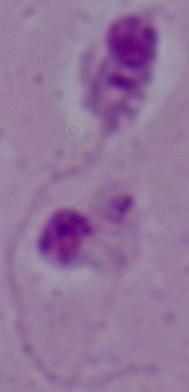
modality: micrograph
magnification: 1000x
identification: Leishmania